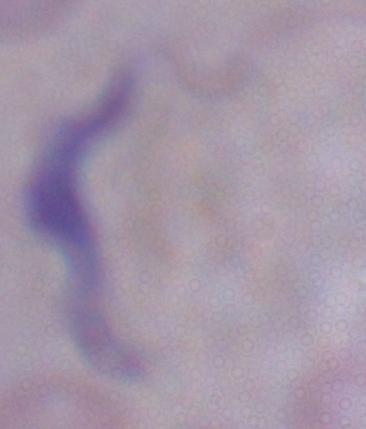

modality = photomicrograph
identification = trypanosome
magnification = 1000x